State the blood parasite species.
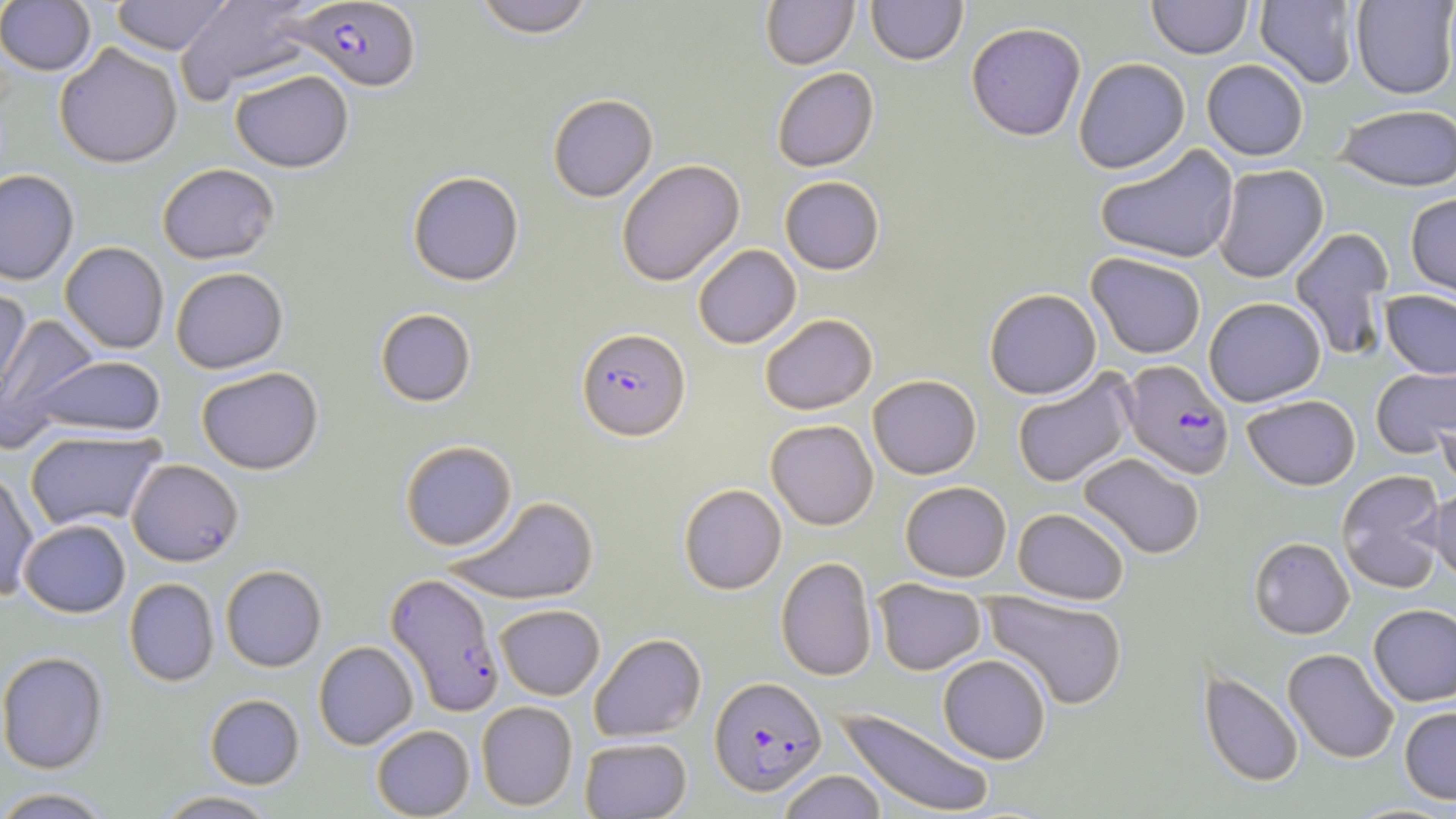
Plasmodium falciparum.

Approximate bounding boxes as [x1, y1, x2, y2] in pixels. Uninfected red blood cell locations: [110, 0, 234, 55], [471, 0, 597, 38], [760, 0, 859, 69], [866, 0, 968, 65], [1146, 0, 1253, 59], [1255, 0, 1360, 88], [1351, 0, 1456, 99], [0, 1, 97, 76], [175, 1, 319, 102], [966, 22, 1086, 140], [54, 42, 183, 168], [1073, 57, 1191, 174], [1201, 59, 1309, 161], [772, 67, 879, 172], [229, 69, 354, 172], [547, 93, 658, 202], [1334, 103, 1456, 192], [1095, 144, 1240, 264], [616, 159, 745, 287], [156, 163, 279, 264], [1211, 163, 1329, 283], [0, 168, 79, 285], [407, 171, 524, 286], [779, 175, 885, 275], [1406, 192, 1456, 303], [1289, 226, 1395, 361], [59, 241, 169, 353], [693, 244, 801, 349], [1086, 252, 1207, 359], [170, 267, 288, 373], [0, 287, 32, 413], [984, 288, 1102, 399], [1380, 290, 1456, 379], [1203, 297, 1326, 407], [375, 308, 476, 407], [0, 310, 100, 443], [759, 313, 878, 415], [30, 355, 167, 438], [1371, 364, 1455, 458], [196, 366, 324, 474], [1011, 369, 1137, 488], [867, 374, 982, 479], [1435, 388, 1456, 492], [1242, 394, 1361, 490], [765, 419, 879, 530], [24, 428, 167, 532], [400, 440, 518, 551], [1077, 452, 1206, 560], [126, 459, 244, 566], [0, 468, 39, 600], [1335, 469, 1447, 593], [900, 481, 1012, 582], [678, 484, 787, 595], [1428, 484, 1456, 585], [445, 495, 599, 605], [1012, 507, 1130, 604], [18, 519, 131, 618], [1249, 537, 1354, 639], [776, 557, 877, 682], [220, 565, 327, 672], [124, 578, 220, 686], [872, 578, 987, 676], [982, 592, 1128, 710], [1368, 603, 1456, 706], [495, 604, 605, 700], [589, 633, 707, 743], [313, 641, 418, 750], [1282, 648, 1400, 763], [0, 651, 109, 773], [938, 654, 1051, 764], [1198, 669, 1304, 788], [204, 694, 305, 789], [476, 701, 578, 811], [1399, 706, 1456, 804], [836, 707, 996, 818], [370, 724, 475, 818], [580, 736, 692, 818], [776, 770, 887, 819], [0, 786, 115, 818], [153, 789, 280, 818], [1341, 802, 1456, 819]. Plasmodium falciparum-infected red blood cell locations: [291, 2, 422, 92], [576, 328, 690, 441], [1120, 359, 1234, 479], [384, 573, 504, 716], [709, 676, 827, 795]. Thin blood smear. Captured at 1000x magnification. Single field of view. Image is 1456×819 pixels. Optical microscopy. May-Grünwald-Giemsa stain.